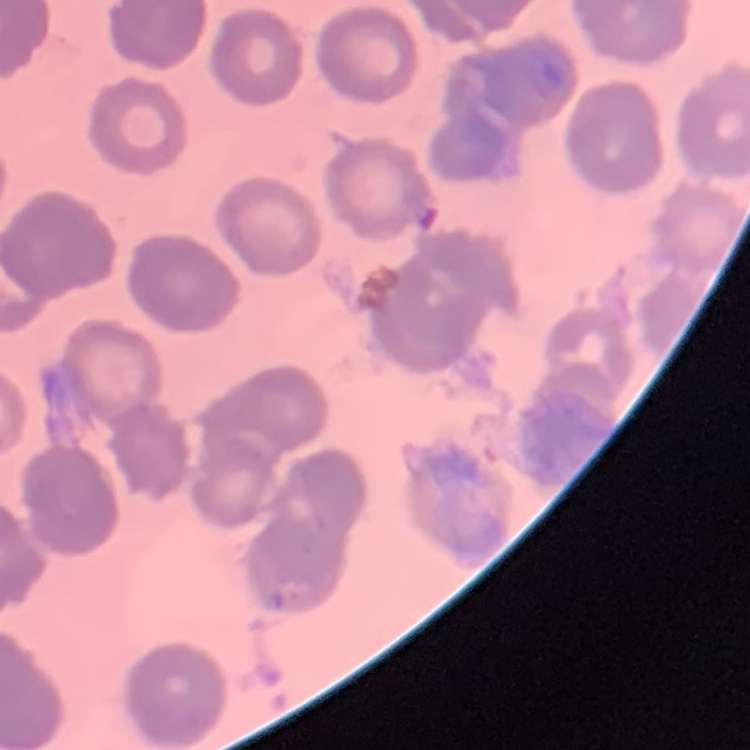
{
  "erythrocyte_morphology": "rouleaux formation",
  "stain": "Field's or Giemsa",
  "preparation": "thin blood film",
  "image_type": "square crop of a larger photomicrograph"
}